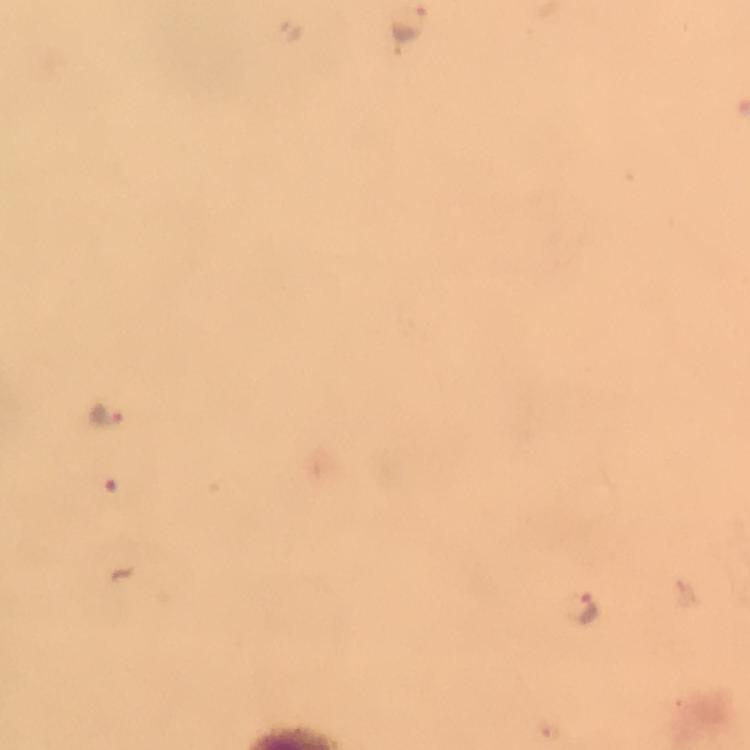

immersion oil = used
preparation = thick smear
magnification = 100x
capture = smartphone camera through the microscope
stain = Giemsa
image size = 750×750 pixels
cropped from = a single field of view
context = from a diagnostic examination for malaria
Plasmodium parasite locations = approximate centers as [x, y] in pixels: [410, 28], [105, 416], [587, 608]